Assess the morphology of the erythrocytes.
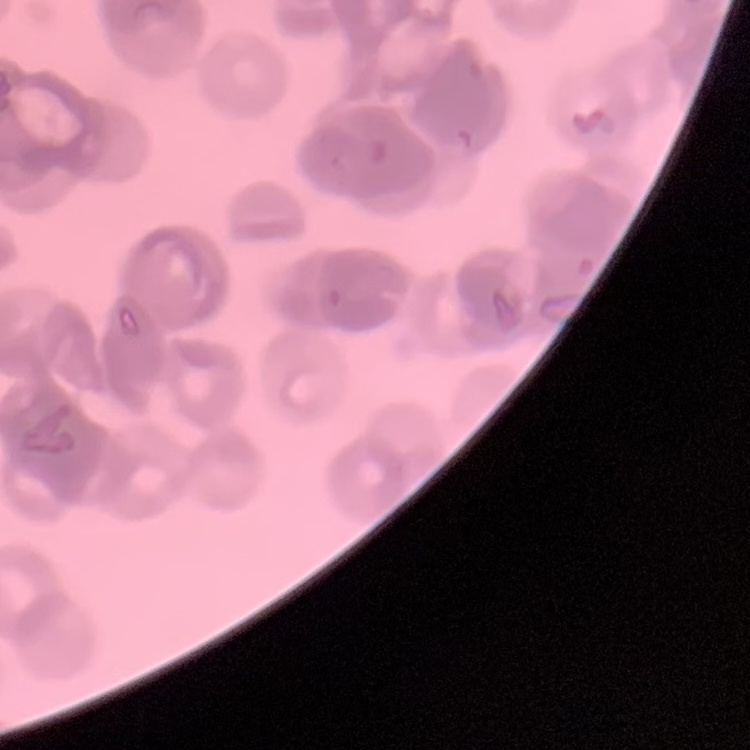

Rouleaux formation.

preparation = thin peripheral smear
stain = Field's or Giemsa
image type = one tile cut from a larger photomicrograph